Report the malaria status of this cell.
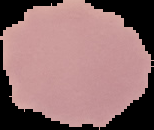

It is uninfected.

From a thin blood smear. Image is 154×130 pixels. Segmented cell region on a black background.